Locate every blood parasite and identify its species.
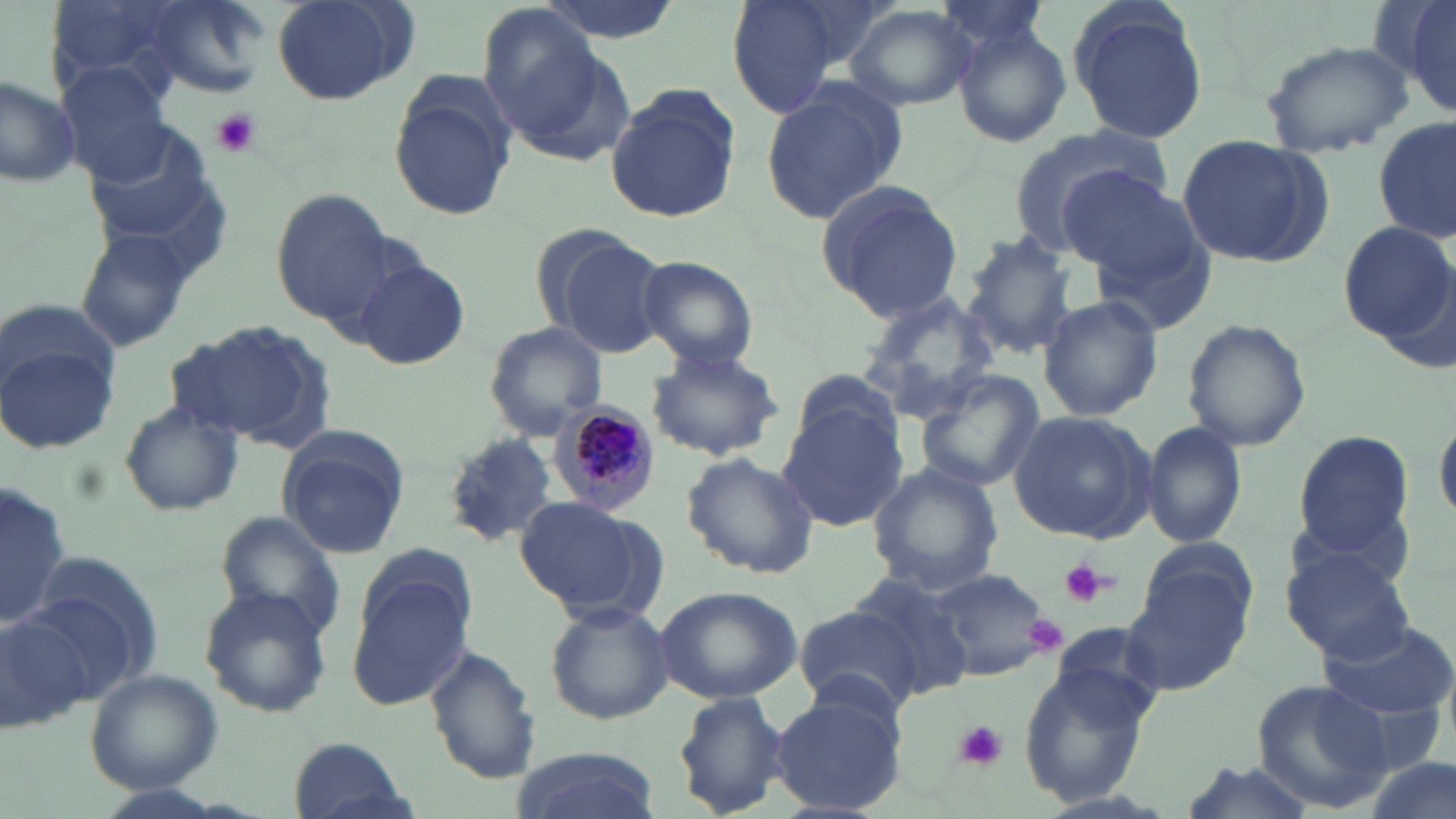

Approximate bounding boxes as named x1/y1/x2/y2 corners in pixels.
Plasmodium malariae-infected red blood cells: (x1=551, y1=401, x2=661, y2=514).
No Plasmodium falciparum, Plasmodium ovale, Plasmodium vivax, Babesia divergens, or Trypanosoma brucei observed.

slide-level diagnosis = Plasmodium malariae
stain = May-Grünwald-Giemsa
image size = 1456×819 pixels
field of view = one of a larger specimen
uninfected red blood cell locations = approximate bounding boxes as named x1/y1/x2/y2 corners in pixels: (x1=141, y1=0, x2=270, y2=99), (x1=531, y1=0, x2=682, y2=43), (x1=725, y1=0, x2=840, y2=118), (x1=1066, y1=0, x2=1209, y2=146), (x1=269, y1=1, x2=418, y2=106), (x1=43, y1=2, x2=189, y2=105), (x1=1404, y1=2, x2=1456, y2=116), (x1=844, y1=4, x2=977, y2=111), (x1=474, y1=5, x2=609, y2=143), (x1=953, y1=20, x2=1071, y2=149), (x1=1260, y1=39, x2=1414, y2=156), (x1=57, y1=66, x2=177, y2=186), (x1=0, y1=74, x2=82, y2=187), (x1=390, y1=77, x2=517, y2=222), (x1=757, y1=83, x2=906, y2=227), (x1=605, y1=85, x2=740, y2=223), (x1=1375, y1=114, x2=1455, y2=245), (x1=1007, y1=121, x2=1175, y2=256), (x1=1176, y1=134, x2=1332, y2=270), (x1=1056, y1=164, x2=1210, y2=292), (x1=814, y1=181, x2=965, y2=323), (x1=270, y1=188, x2=400, y2=326), (x1=1335, y1=221, x2=1455, y2=346), (x1=75, y1=228, x2=198, y2=353), (x1=545, y1=231, x2=670, y2=355), (x1=961, y1=231, x2=1081, y2=360), (x1=349, y1=253, x2=471, y2=372), (x1=635, y1=256, x2=760, y2=370), (x1=856, y1=291, x2=1001, y2=427), (x1=1037, y1=295, x2=1164, y2=422), (x1=3, y1=299, x2=123, y2=405), (x1=1182, y1=318, x2=1314, y2=452), (x1=168, y1=321, x2=334, y2=450), (x1=482, y1=322, x2=608, y2=440), (x1=2, y1=336, x2=121, y2=452), (x1=645, y1=346, x2=789, y2=459), (x1=791, y1=367, x2=903, y2=460), (x1=912, y1=370, x2=1045, y2=493), (x1=118, y1=399, x2=244, y2=518), (x1=778, y1=404, x2=910, y2=531), (x1=1006, y1=408, x2=1153, y2=543), (x1=1435, y1=409, x2=1456, y2=529), (x1=1140, y1=421, x2=1248, y2=549), (x1=275, y1=427, x2=409, y2=559), (x1=1293, y1=430, x2=1418, y2=562), (x1=439, y1=434, x2=555, y2=549), (x1=682, y1=453, x2=819, y2=579), (x1=867, y1=463, x2=1004, y2=596), (x1=0, y1=480, x2=73, y2=632), (x1=513, y1=498, x2=660, y2=617), (x1=216, y1=509, x2=349, y2=640), (x1=1280, y1=541, x2=1417, y2=665), (x1=1128, y1=549, x2=1255, y2=690), (x1=24, y1=551, x2=161, y2=699), (x1=924, y1=569, x2=1052, y2=680), (x1=347, y1=573, x2=473, y2=712), (x1=847, y1=576, x2=977, y2=699), (x1=654, y1=585, x2=804, y2=704), (x1=198, y1=587, x2=332, y2=718), (x1=546, y1=602, x2=673, y2=724), (x1=0, y1=605, x2=97, y2=736), (x1=794, y1=607, x2=923, y2=715), (x1=1317, y1=616, x2=1456, y2=719), (x1=423, y1=643, x2=542, y2=783), (x1=1015, y1=659, x2=1156, y2=809), (x1=85, y1=669, x2=222, y2=792), (x1=1248, y1=679, x2=1394, y2=812), (x1=771, y1=686, x2=909, y2=817), (x1=672, y1=689, x2=791, y2=818), (x1=288, y1=735, x2=413, y2=819), (x1=508, y1=748, x2=662, y2=819), (x1=1358, y1=755, x2=1453, y2=819), (x1=1174, y1=761, x2=1318, y2=819)
platelet locations = approximate bounding boxes as named x1/y1/x2/y2 corners in pixels: (x1=210, y1=108, x2=262, y2=159), (x1=1058, y1=558, x2=1109, y2=608), (x1=1021, y1=614, x2=1069, y2=657), (x1=954, y1=718, x2=1008, y2=771)
preparation = thin blood film
magnification = 1000x
modality = light microscopy